Name the parasite shown.
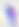

This is Toxoplasma gondii.

Summary:
  - Magnification: 400x
  - Modality: photomicrograph